Report the malaria status.
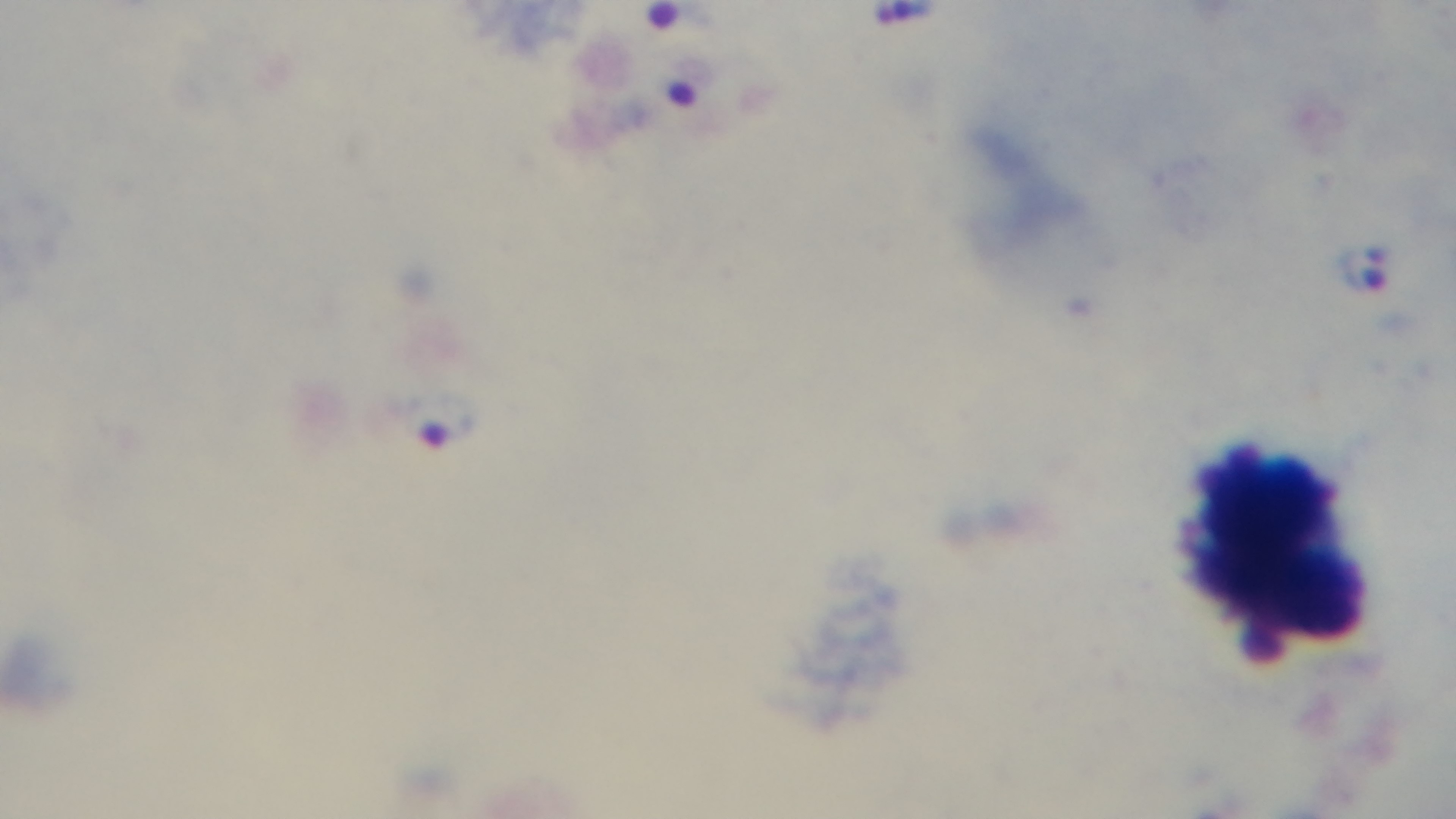

Infected.

Summary:
  - Stain: Giemsa
  - Capture: mounted 4K digital camera
  - Objective: 100x oil immersion
  - Field of view: one from the slide
  - Preparation: thick smear
  - Modality: light microscopy